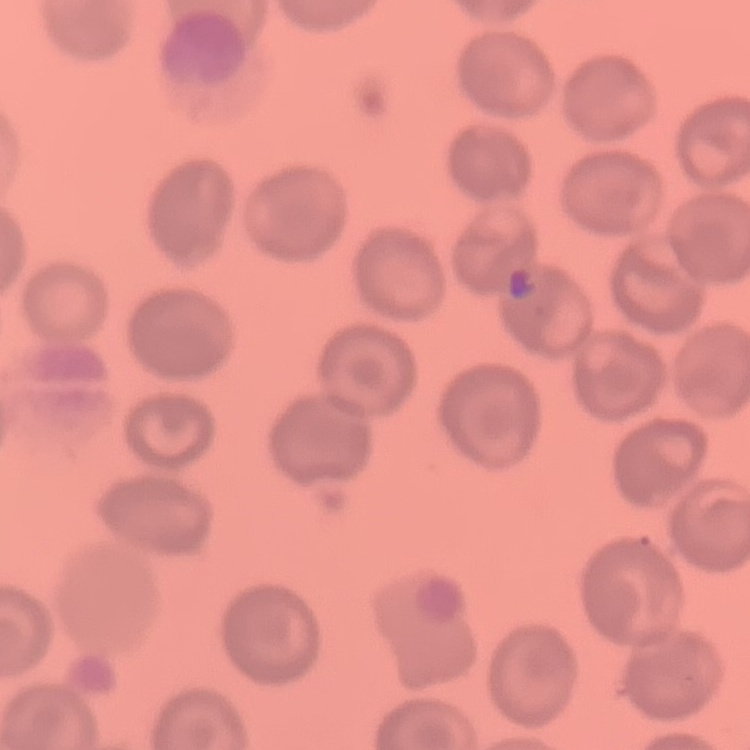

red blood cell morphology = no rouleaux formation
image type = one tile cut from a larger photomicrograph
stain = Field's or Giemsa
preparation = thin blood film